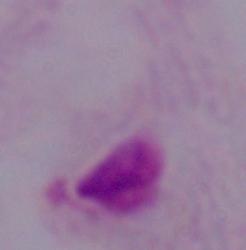
identification = trichomonad
modality = micrograph
magnification = 1000x